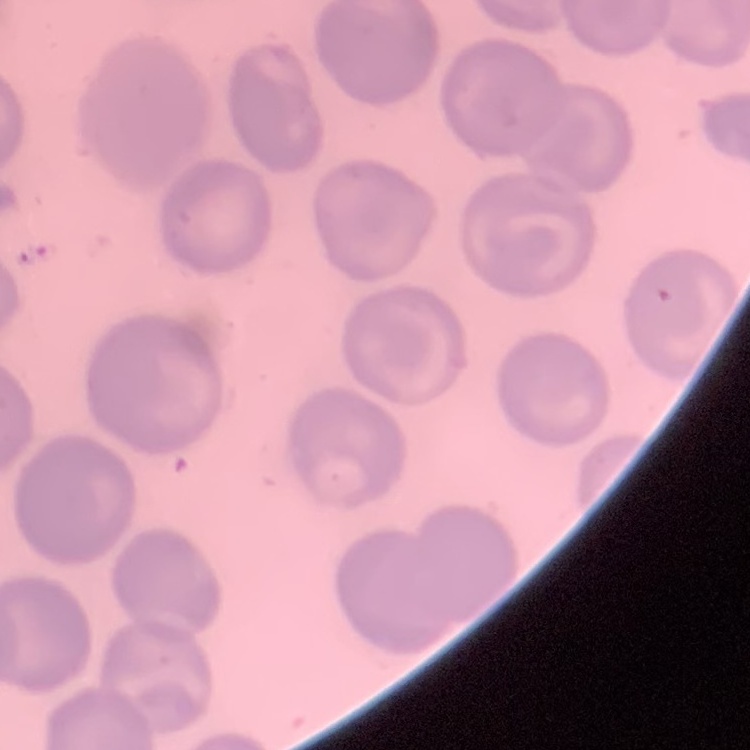 The red blood cells show no rouleaux formation. Thin blood smear. Field's or Giemsa stain. Square crop of a larger photomicrograph.